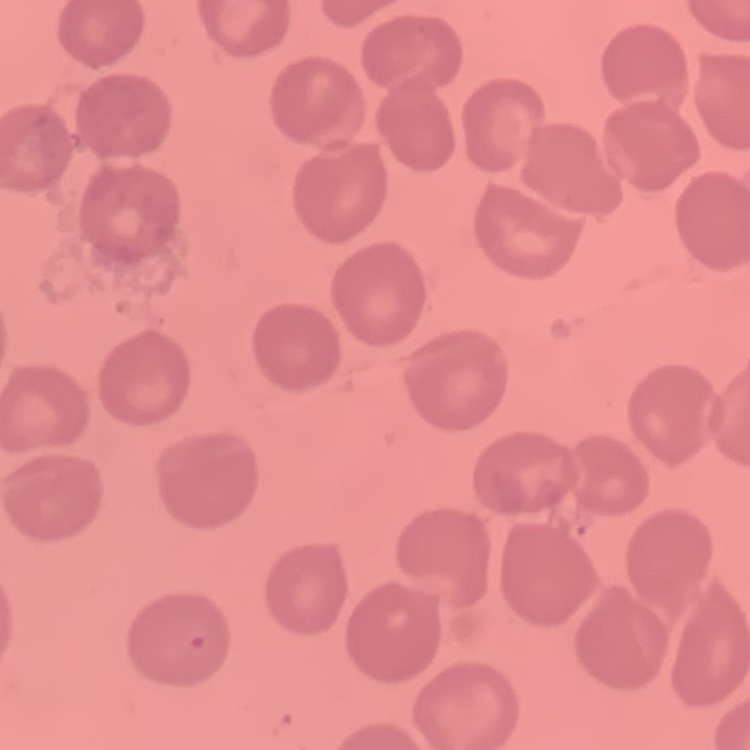
Summary:
  - Erythrocyte morphology: no rouleaux formation
  - Stain: Field's or Giemsa
  - Preparation: thin blood smear
  - Image type: one tile cut from a larger photomicrograph